Assess this cell for malaria.
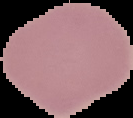

Uninfected.

Summary:
  - Image size: 133×118 pixels
  - Preparation: thin blood film
  - Image type: segmented cell region on a black background